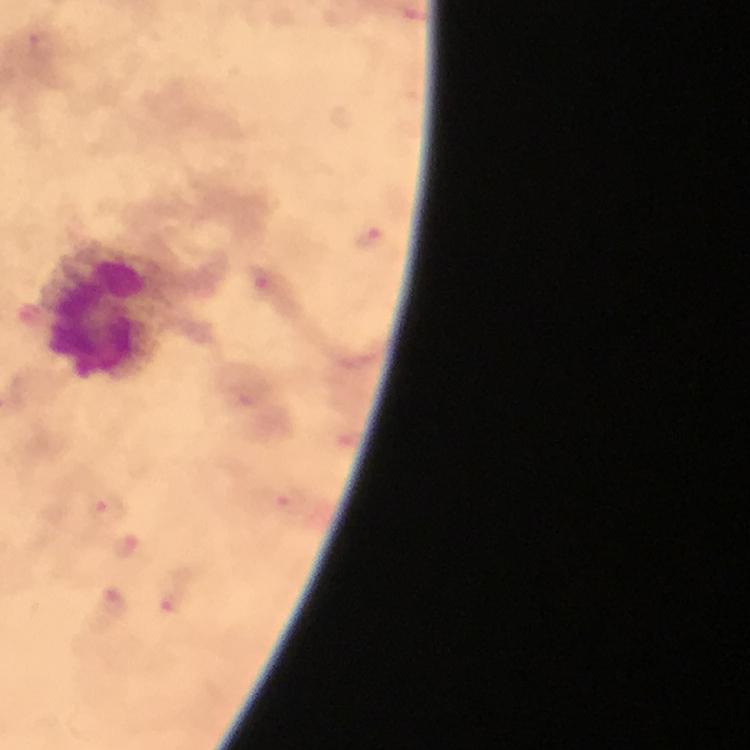

Plasmodium parasite locations = approximate object centers, in pixels from the top-left corner: (x=367, y=239), (x=264, y=281), (x=287, y=501), (x=102, y=511), (x=129, y=546), (x=170, y=593), (x=114, y=603)
context = from a malaria diagnostic workup
magnification = 100x
capture = smartphone photograph through a microscope
stain = Giemsa
leukocyte locations = approximate object centers, in pixels from the top-left corner: (x=100, y=314)
cropped from = a single field of view
preparation = thick blood smear
immersion oil = used
image size = 750×750 pixels